Classify this cell by malaria status.
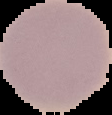

It is uninfected.

Summary:
  - Preparation: thin blood film
  - Image type: segmented cell region on a black background
  - Image size: 112×115 pixels